Assess this cell for malaria.
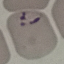

It is parasitized.

capture: smartphone through the microscope eyepiece
preparation: thin blood smear
image_type: automatically extracted cell patch, resized to 64 × 64 pixels
stain: Giemsa